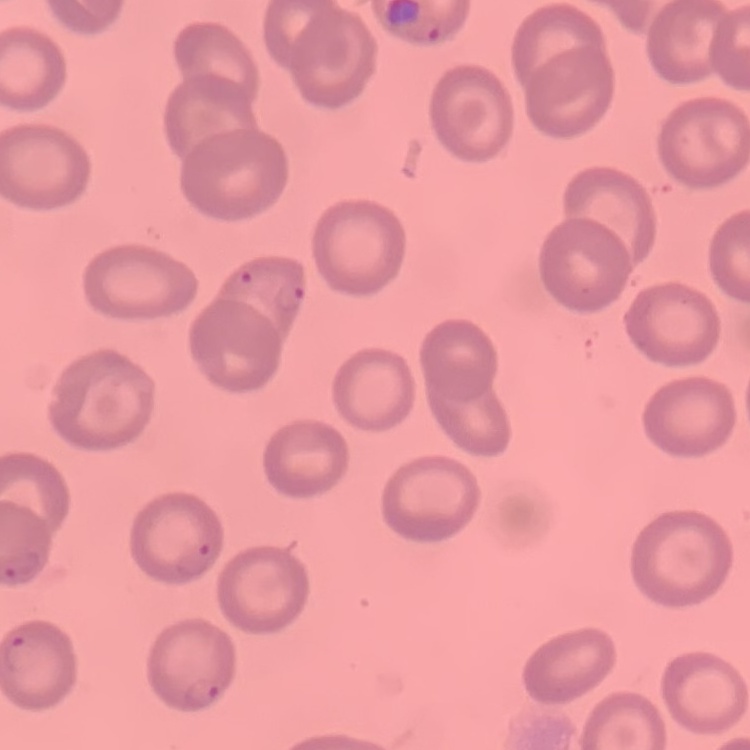

{
  "erythrocyte_morphology": "no rouleaux formation",
  "preparation": "thin blood smear",
  "stain": "Field's or Giemsa",
  "image_type": "one tile cut from a larger photomicrograph"
}